Locate and identify every blood parasite.
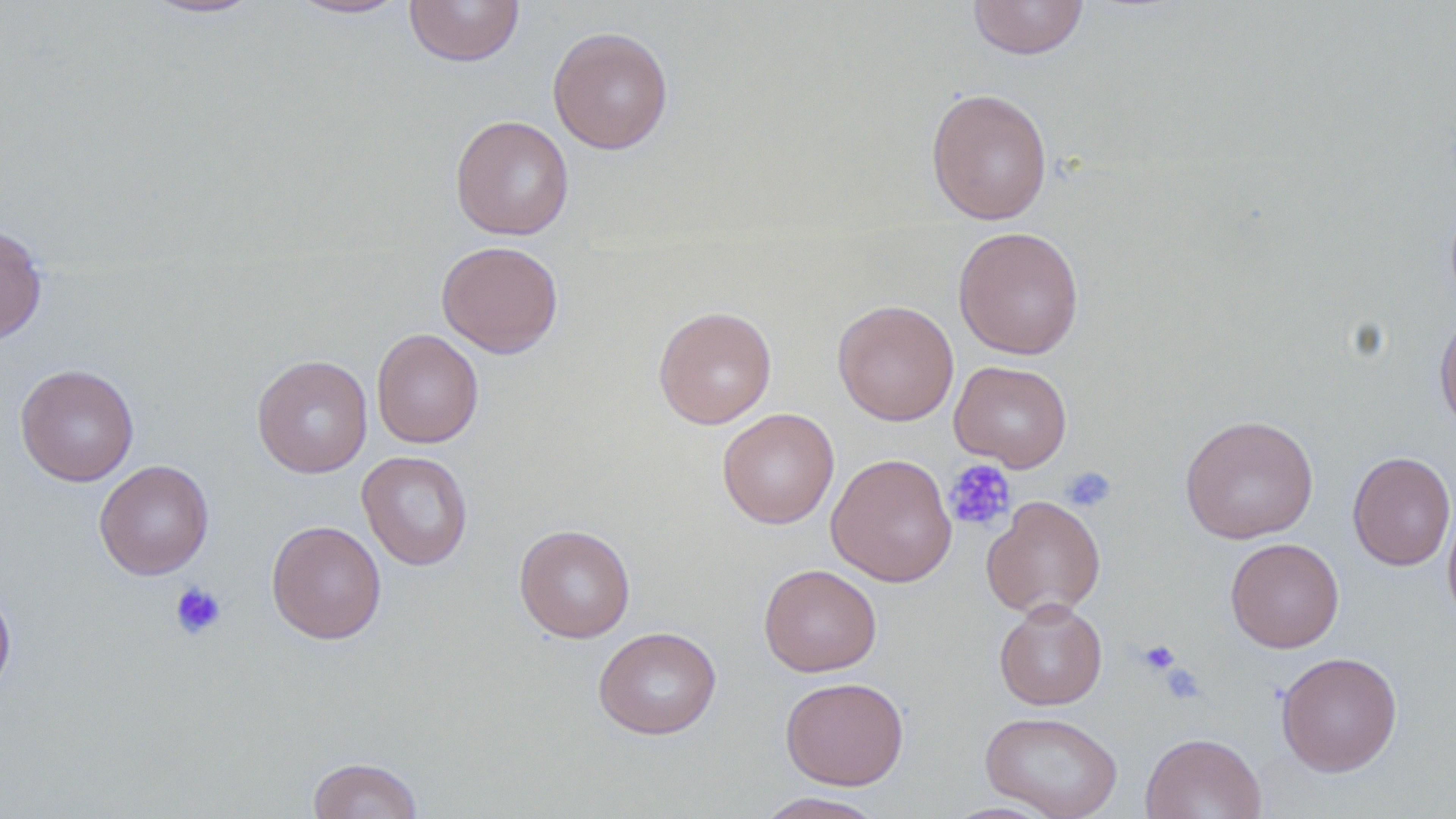
No blood parasites observed.

Summary:
  - Coordinate format: approximate bounding boxes as [x1, y1, x2, y2] in pixels
  - Platelet locations: [944, 459, 1015, 532], [1061, 467, 1117, 513], [170, 581, 226, 640], [1137, 639, 1180, 676], [1157, 661, 1207, 704]
  - Uninfected red blood cell locations: [141, 0, 265, 19], [288, 0, 411, 19], [404, 0, 525, 67], [967, 0, 1089, 60], [547, 27, 674, 154], [925, 87, 1053, 226], [450, 115, 574, 240], [0, 224, 47, 344], [953, 225, 1084, 360], [436, 240, 564, 358], [833, 299, 959, 426], [653, 305, 777, 429], [1434, 310, 1456, 437], [371, 328, 484, 448], [252, 354, 373, 478], [949, 360, 1073, 472], [15, 364, 139, 486], [716, 408, 839, 529], [1180, 414, 1319, 543], [357, 450, 474, 570], [1348, 451, 1455, 571], [826, 452, 958, 587], [94, 460, 214, 580], [981, 495, 1106, 619], [1442, 497, 1456, 628], [266, 520, 387, 644], [514, 524, 636, 642], [1225, 537, 1344, 653], [758, 563, 882, 677], [0, 581, 16, 702], [994, 599, 1108, 710], [593, 626, 722, 739], [1276, 651, 1403, 776], [781, 676, 909, 790], [979, 710, 1123, 819], [1140, 732, 1267, 819], [307, 757, 424, 819], [752, 792, 889, 819]
  - Slide-level diagnosis: no evidence of blood parasites
  - Preparation: thin blood film
  - Field of view: one of a larger specimen
  - Modality: optical microscopy
  - Image size: 1456×819 pixels
  - Stain: May-Grünwald-Giemsa
  - Magnification: 1000x